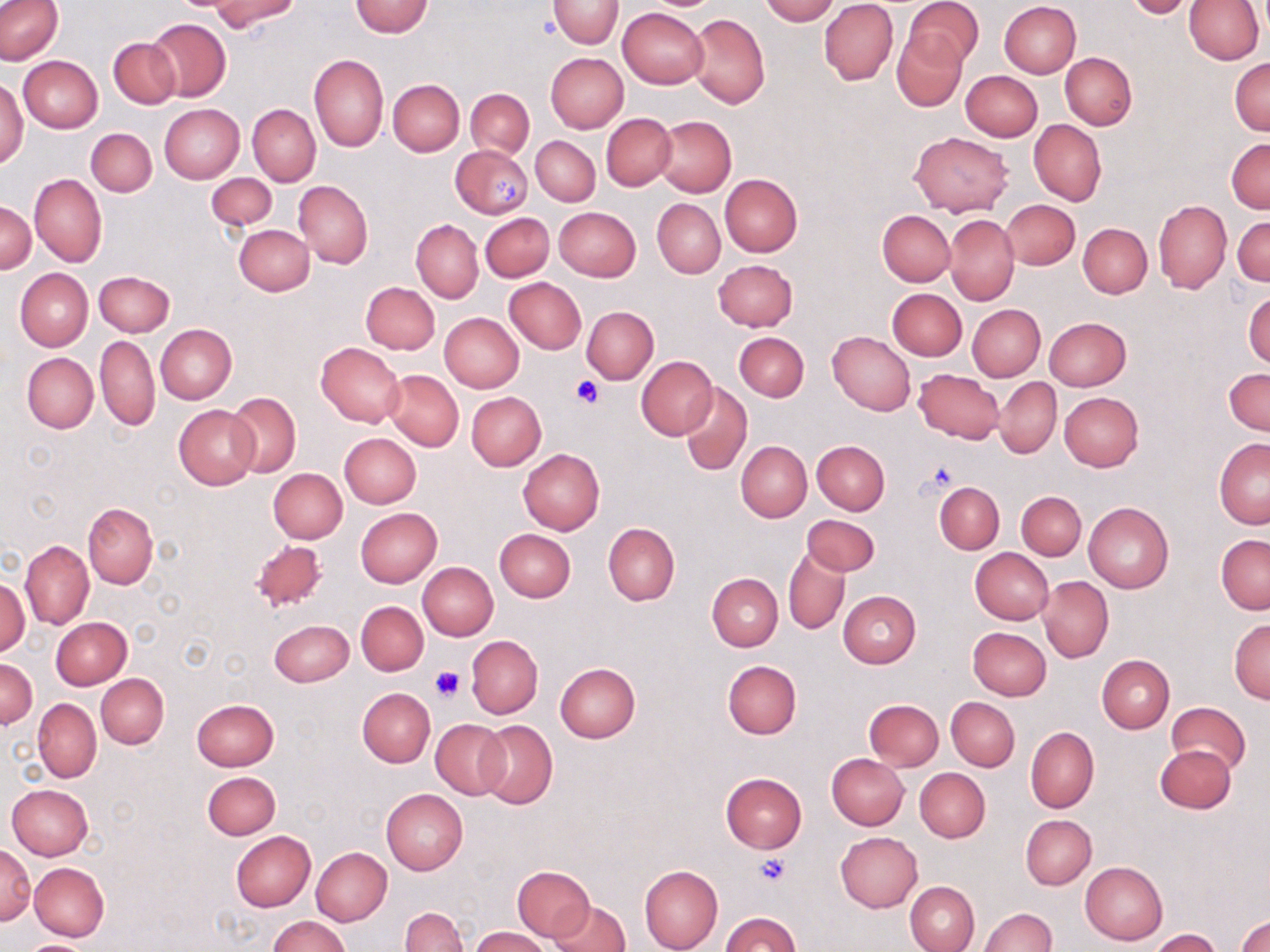

Approximate bounding boxes as (x1,y1)-(x2,y2) corner pairs in pixels. Uninfected red blood cell locations: (210,0)-(299,32), (548,0)-(623,48), (759,0)-(837,24), (820,0)-(898,85), (906,0)-(982,70), (1122,0)-(1197,18), (350,1)-(434,37), (999,1)-(1082,78), (1184,1)-(1264,64), (0,2)-(64,64), (618,8)-(708,89), (687,14)-(771,109), (147,18)-(231,102), (892,29)-(967,111), (108,36)-(181,110), (308,53)-(388,152), (546,53)-(628,133), (1061,53)-(1137,128), (18,55)-(103,133), (1229,58)-(1270,135), (961,71)-(1043,141), (0,76)-(28,168), (387,79)-(464,156), (464,88)-(534,158), (160,104)-(244,184), (248,104)-(320,186), (602,115)-(676,189), (654,116)-(736,197), (1028,119)-(1106,207), (86,129)-(156,197), (909,132)-(1013,216), (531,136)-(601,205), (1227,139)-(1270,213), (449,145)-(533,218), (206,173)-(277,231), (719,174)-(802,256), (30,175)-(106,267), (293,180)-(373,267), (653,199)-(725,279), (1002,199)-(1080,269), (0,200)-(36,273), (1154,201)-(1231,293), (554,207)-(641,282), (877,211)-(955,286), (486,212)-(559,347), (480,213)-(553,281), (944,213)-(1019,306), (1232,215)-(1269,286), (411,219)-(482,303), (1078,223)-(1152,298), (234,224)-(314,295), (712,259)-(798,331), (15,268)-(93,351), (99,269)-(170,408), (94,271)-(174,337), (505,278)-(586,353), (361,281)-(440,353), (886,288)-(967,361), (1244,289)-(1270,369), (966,304)-(1045,381), (582,306)-(658,383), (439,312)-(523,393), (1044,316)-(1131,391), (155,324)-(237,404), (735,331)-(809,402), (827,332)-(915,416), (95,334)-(159,431), (316,343)-(405,426), (22,353)-(98,432), (636,356)-(718,441), (1225,368)-(1269,436), (913,369)-(1004,444), (383,370)-(463,450), (995,377)-(1061,457), (678,382)-(752,476), (466,392)-(545,470), (1059,392)-(1143,472), (226,393)-(301,477), (174,405)-(259,488), (339,433)-(421,508), (1214,437)-(1270,528), (736,440)-(811,521), (812,440)-(890,516), (517,448)-(603,534), (268,468)-(347,542), (934,482)-(1003,554), (1017,492)-(1086,560), (83,502)-(158,589), (1083,502)-(1174,593), (355,507)-(442,588), (798,510)-(872,647), (802,514)-(880,575), (603,523)-(679,605), (494,529)-(576,602), (1216,534)-(1269,613), (21,540)-(93,629), (251,540)-(328,612), (783,544)-(850,634), (970,547)-(1052,624), (418,562)-(498,639), (707,573)-(782,651), (1037,576)-(1114,663), (0,577)-(29,655), (837,590)-(921,668), (356,601)-(428,676), (51,618)-(131,690), (268,619)-(354,686), (1229,619)-(1270,702), (968,627)-(1051,700), (466,635)-(542,719), (1097,654)-(1174,733), (1,658)-(37,728), (723,660)-(801,739), (555,662)-(641,743), (96,673)-(168,748), (357,688)-(435,766), (947,697)-(1020,771), (33,698)-(101,782), (191,699)-(278,771), (864,699)-(944,770), (1167,702)-(1250,775), (430,719)-(509,799), (476,720)-(558,810), (1025,727)-(1098,813), (1154,745)-(1235,813), (827,753)-(908,829), (915,768)-(990,841), (203,771)-(280,839), (721,773)-(806,853), (7,784)-(94,860), (382,789)-(468,874), (1021,815)-(1096,889), (231,831)-(316,911), (836,831)-(923,912), (0,844)-(35,924), (311,846)-(391,925), (1080,861)-(1167,945), (29,862)-(109,941), (512,865)-(595,941), (639,865)-(723,952), (905,881)-(979,952), (549,899)-(630,952), (401,907)-(468,952), (978,908)-(1055,952), (722,911)-(799,952), (267,915)-(351,952), (1238,915)-(1270,952), (471,928)-(550,952), (1151,929)-(1221,951), (17,939)-(100,952). Platelet locations: (491,175)-(522,208), (570,375)-(603,408), (917,460)-(959,498), (429,664)-(462,701), (756,855)-(791,886). Slide-level diagnosis: no evidence of blood parasites. May-Grünwald-Giemsa stain. One field of a larger specimen. Thin blood film. Image is 1270×952 pixels. Optical microscopy. Captured at 1000x magnification.